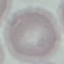
Summary:
  - Malaria status: uninfected
  - Capture: smartphone camera at the microscope eyepiece
  - Stain: Giemsa
  - Image type: automatically extracted cell patch, resized to 64 × 64 pixels
  - Preparation: thin smear